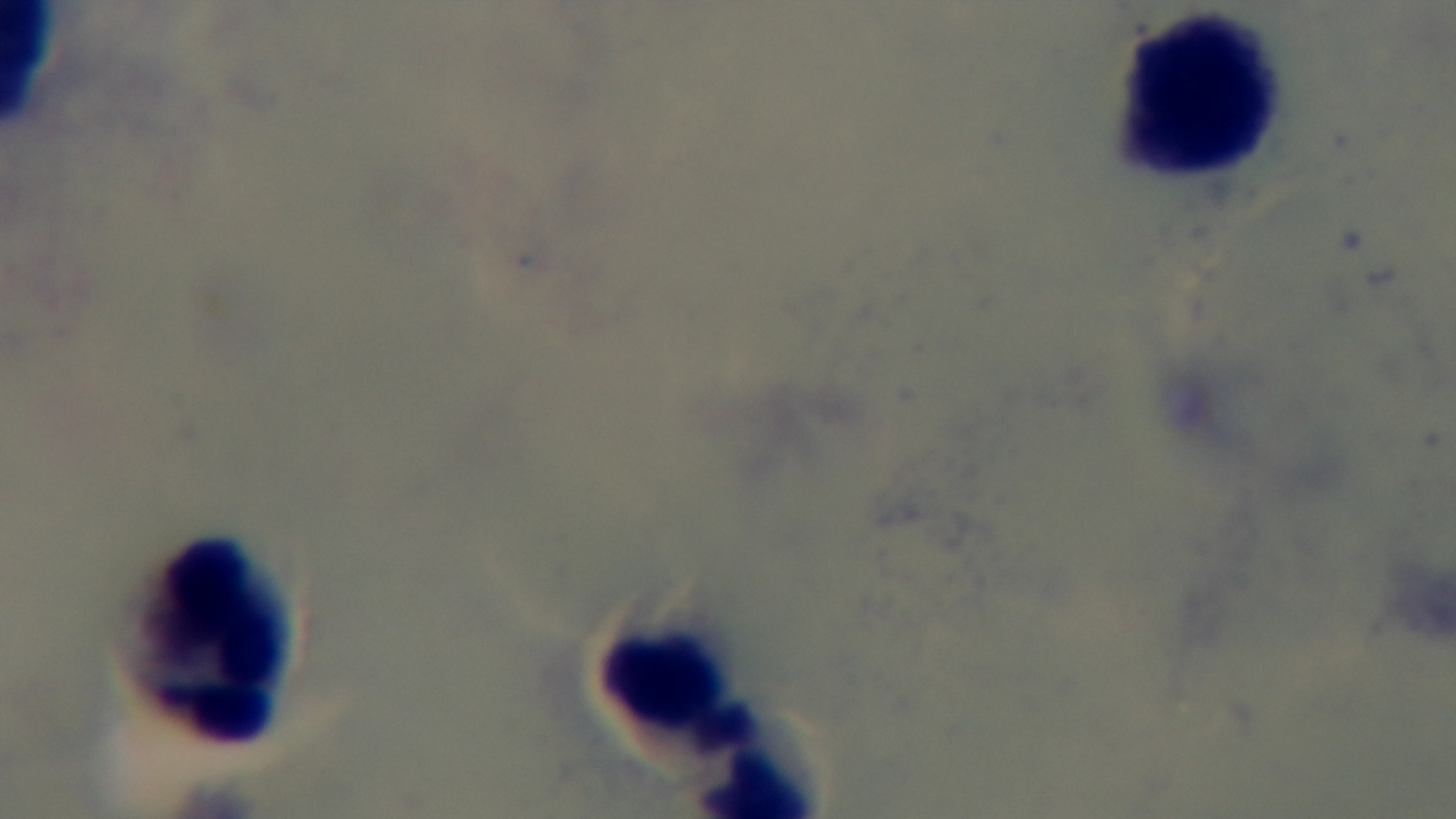
capture = mounted 4K digital camera
preparation = thick smear
malaria status = negative
stain = Giemsa
objective = 100x oil immersion
field of view = one from the slide
modality = light microscopy